Name the parasite shown.
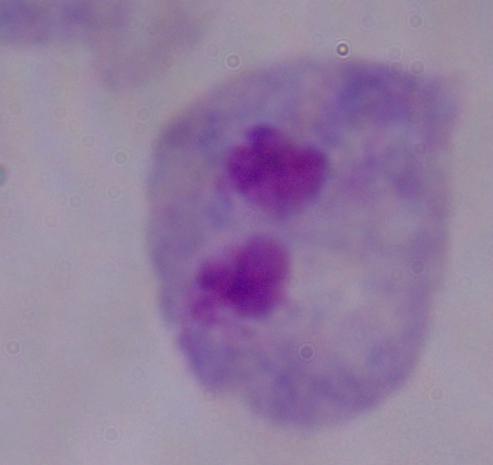
This is a trichomonad.

{
  "modality": "micrograph",
  "magnification": "1000x"
}